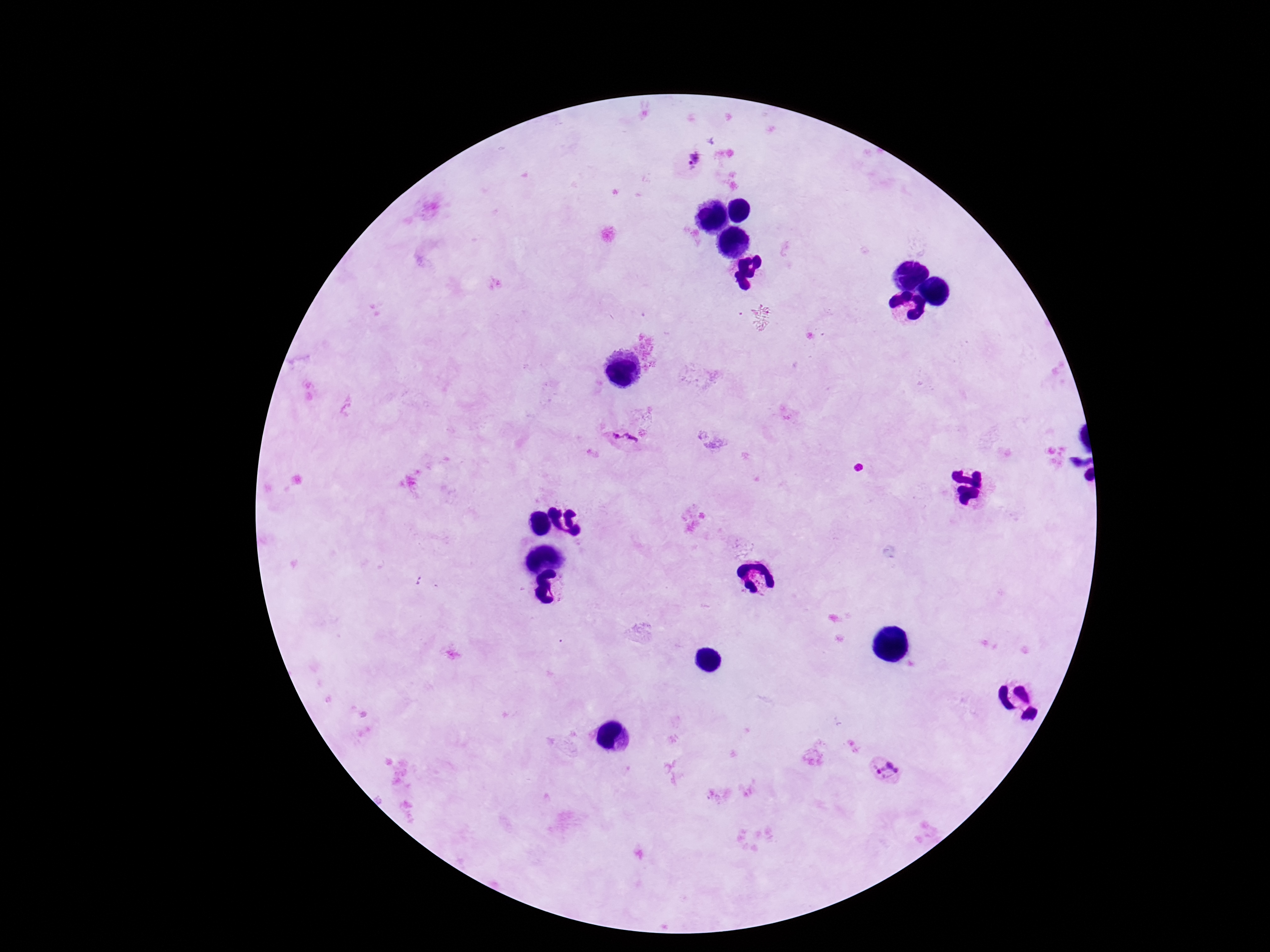

Approximate centers as (x, y) in pixels.
Summary:
  - Plasmodium parasite locations: (694, 162), (624, 440), (888, 769)
  - Image size: 1270×952 pixels
  - Preparation: thick blood film
  - Field of view: single
  - Patient malaria status: positive
  - Magnification: 100x
  - Capture: smartphone camera through the microscope eyepiece
  - Stain: Giemsa